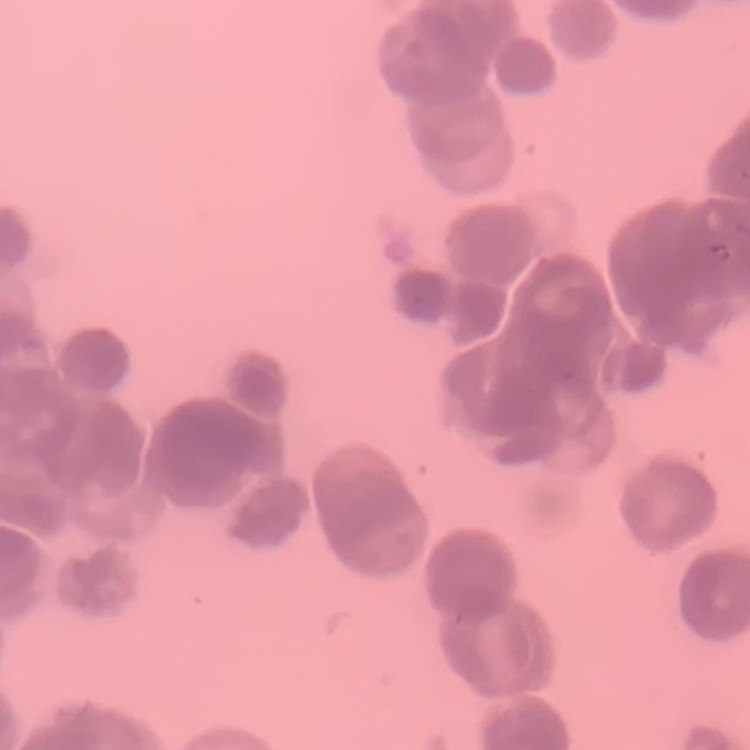
The erythrocytes show rouleaux formation. Field's or Giemsa stain. One tile cut from a larger photomicrograph. Thin peripheral smear.